Give the preparation type.
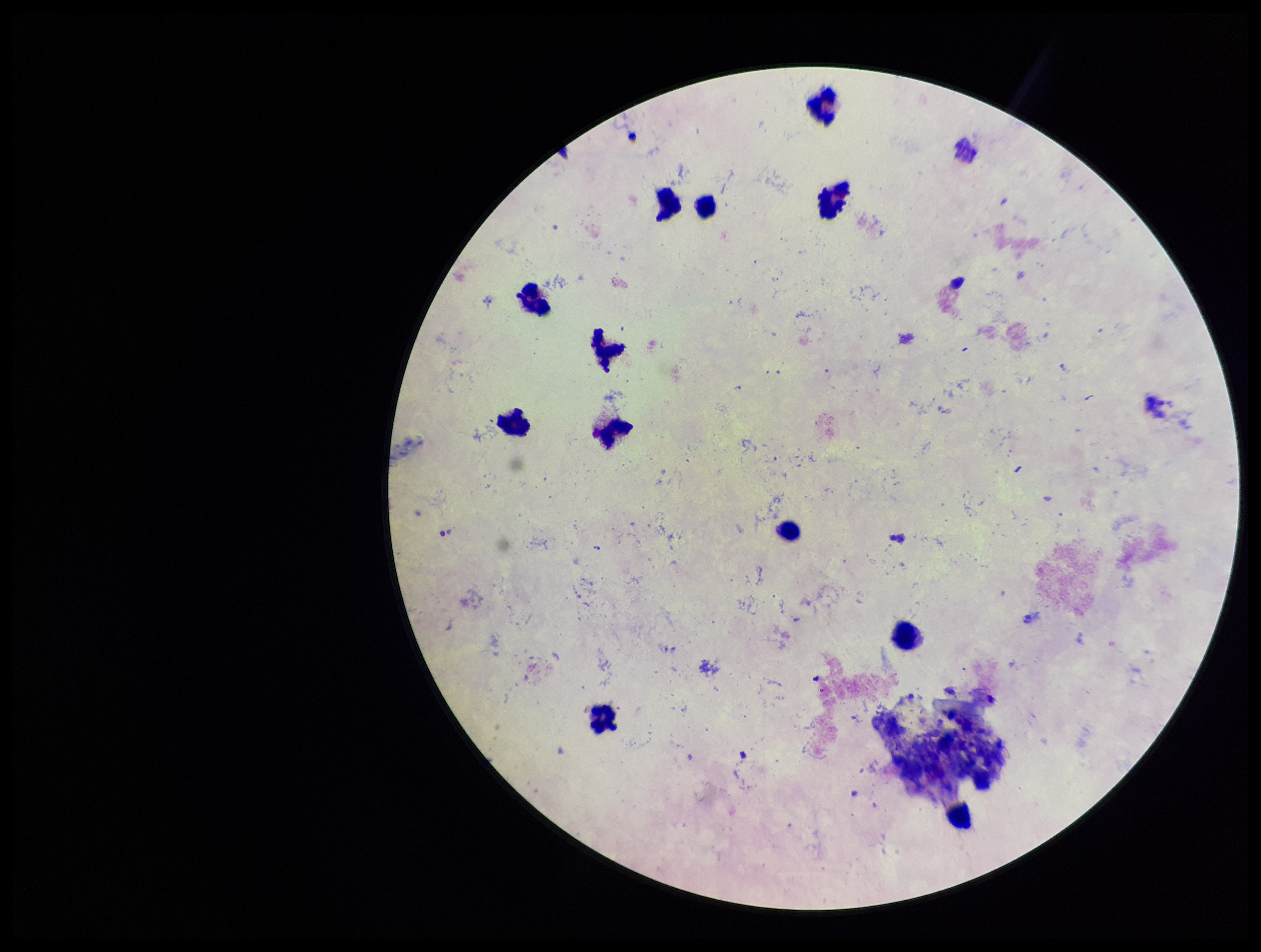
A thick smear.

Image is 1261×952 pixels. Single field of view. Plasmodium parasites: none seen. Photographed through the microscope eyepiece with a smartphone camera. Parasite count: 0. Leukocyte count: 12. Stained with Giemsa. Patient malaria status: negative.